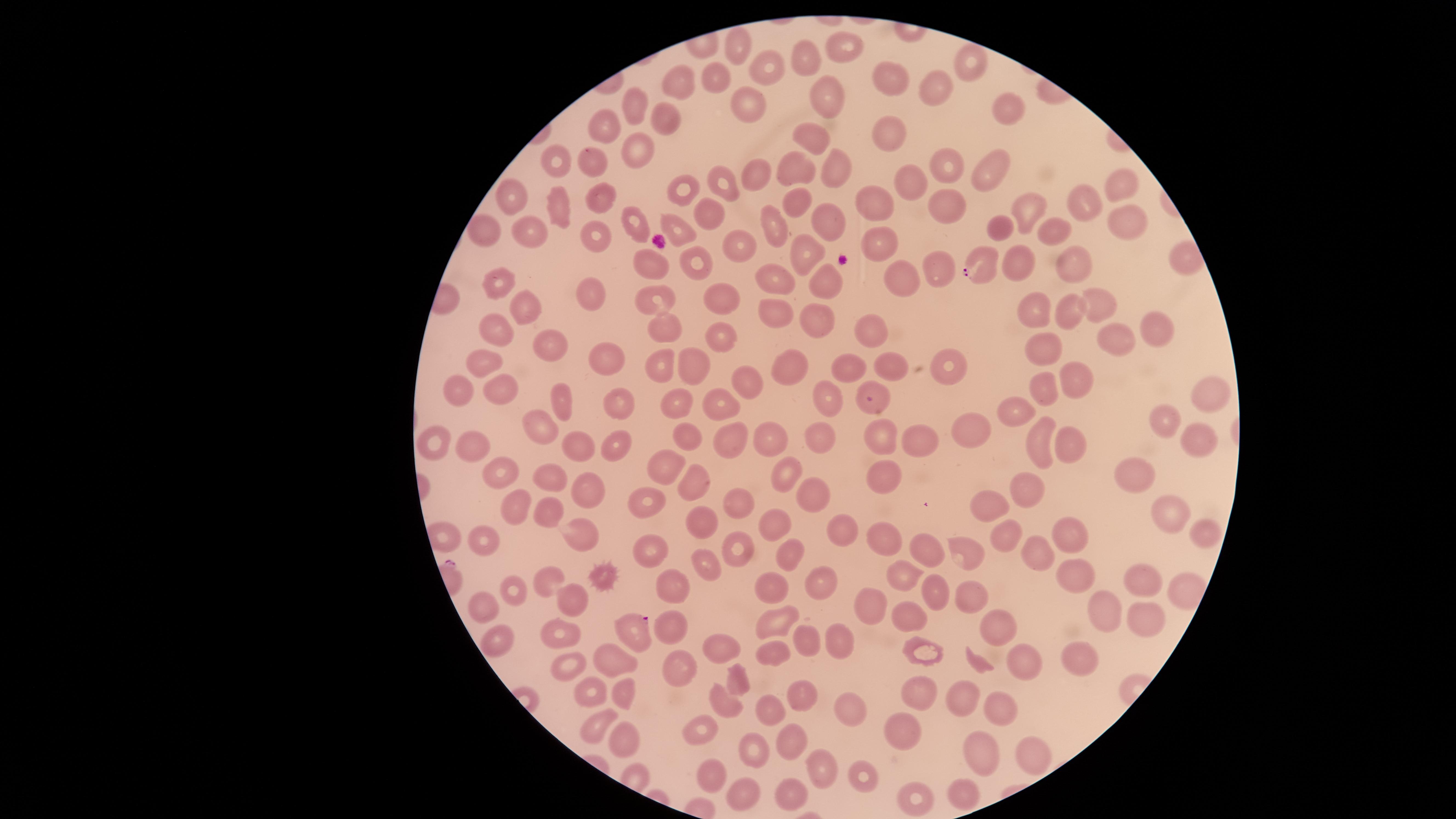
{
  "uninfected_red_blood_cells": "approximate marker points as (x, y) in pixels: (732, 41), (851, 44), (806, 58), (971, 63), (767, 67), (895, 76), (717, 81), (679, 82), (936, 87), (825, 100), (638, 102), (745, 102), (1006, 105), (667, 123), (602, 124), (885, 130), (812, 134), (641, 154), (593, 160), (554, 162), (834, 168), (942, 168), (794, 173), (757, 177), (993, 177), (908, 180), (721, 182), (1124, 182), (683, 190), (513, 195), (604, 199), (1083, 201), (795, 203), (869, 203), (1024, 207), (563, 210), (710, 210), (944, 211), (825, 217), (1118, 218), (632, 224), (676, 226), (479, 227), (777, 230), (1002, 230), (531, 232), (599, 233), (1050, 234), (879, 242), (741, 248), (803, 252), (1072, 258), (1184, 260), (695, 261), (651, 264), (1022, 265), (939, 271), (903, 280), (775, 281), (504, 282), (822, 285), (590, 296), (655, 296), (727, 296), (1100, 302), (529, 308), (770, 308), (1032, 308), (1072, 308), (1151, 325), (816, 326), (665, 327), (490, 329), (876, 334), (721, 338), (547, 342), (1113, 343), (1044, 348), (607, 361), (695, 363), (481, 364), (661, 365), (846, 367), (890, 368), (945, 368), (795, 371), (1072, 377), (747, 380), (1042, 386), (499, 387), (454, 390), (826, 393), (1205, 396), (876, 397), (564, 400), (619, 402), (723, 404), (677, 407), (1014, 410), (1163, 421), (539, 427), (972, 430), (733, 434), (816, 434), (769, 435), (688, 436), (877, 439), (573, 440), (915, 440), (1195, 441), (616, 442), (1069, 442), (437, 443), (473, 444), (1038, 446), (670, 463), (503, 469), (787, 474), (1137, 475), (888, 476), (552, 477), (696, 483), (1025, 485), (585, 489), (812, 492), (644, 498), (735, 502), (506, 506), (993, 508), (543, 511), (1170, 511), (706, 520), (773, 524), (835, 527), (449, 531), (1065, 533), (1207, 533), (583, 536), (877, 537), (1006, 538), (486, 540), (738, 544), (644, 550), (919, 550), (1034, 551), (784, 552), (965, 553), (706, 565), (1069, 574), (909, 577), (545, 579), (821, 579), (1137, 579), (672, 582), (606, 583), (510, 585), (769, 588), (1182, 590), (937, 594), (969, 594), (568, 596), (488, 607), (867, 607), (1102, 614), (907, 616), (768, 620), (668, 623), (1148, 625), (552, 629), (1001, 632), (805, 635), (835, 637), (496, 638), (716, 645), (768, 652), (928, 653), (615, 659), (1028, 659), (673, 665), (1076, 665), (573, 666), (590, 687), (743, 688), (623, 693), (923, 694), (802, 696), (721, 699), (960, 701), (847, 704), (1000, 707), (769, 710), (698, 727), (905, 731), (594, 732), (792, 739), (629, 740), (1027, 747), (755, 748), (977, 751), (816, 762), (709, 769), (859, 773), (963, 792), (792, 795), (743, 796), (917, 796)",
  "species": "Plasmodium falciparum",
  "visible_region": "circular",
  "parasitized_red_blood_cells": "approximate marker points as (x, y) in pixels: (981, 267), (634, 629)",
  "capture": "smartphone photograph through the microscope eyepiece",
  "preparation": "thin blood film",
  "stain": "Giemsa",
  "presence": "malaria parasites identified",
  "field_of_view": "single",
  "image_size": "1456×819 pixels"
}